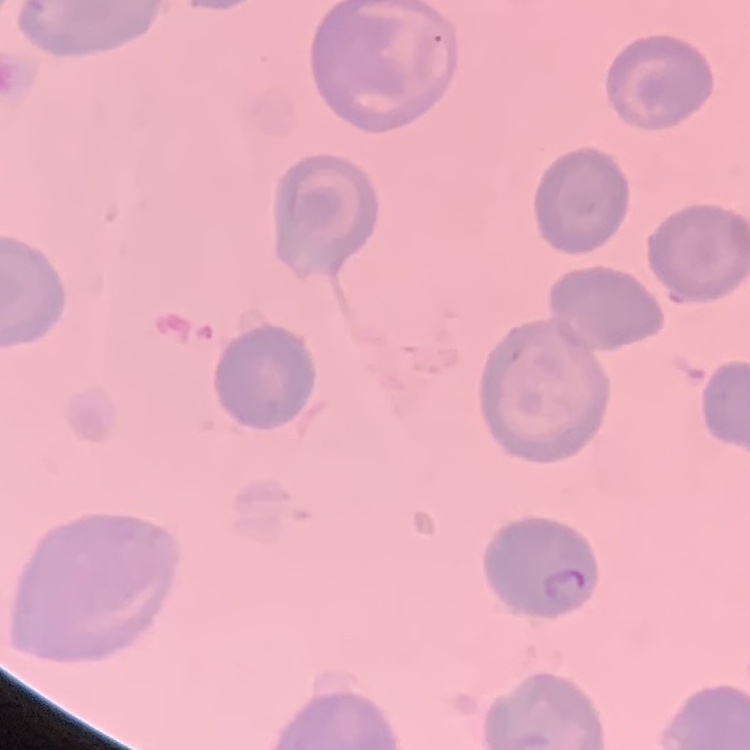

Summary:
  - Red blood cell morphology: no rouleaux formation
  - Stain: Field's or Giemsa
  - Image type: one tile cut from a larger photomicrograph
  - Preparation: thin blood film